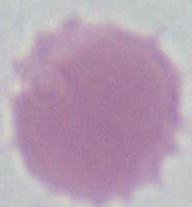 Captured at 1000x magnification. Photomicrograph. A red blood cell is seen.